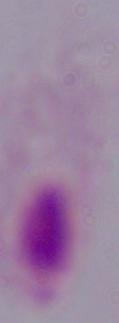

Summary:
  - Modality: micrograph
  - Magnification: 1000x
  - Identification: trichomonad